Identify the cell.
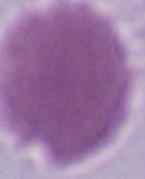
This is an erythrocyte.

{
  "modality": "micrograph",
  "magnification": "1000x"
}